Describe the morphology of the erythrocytes.
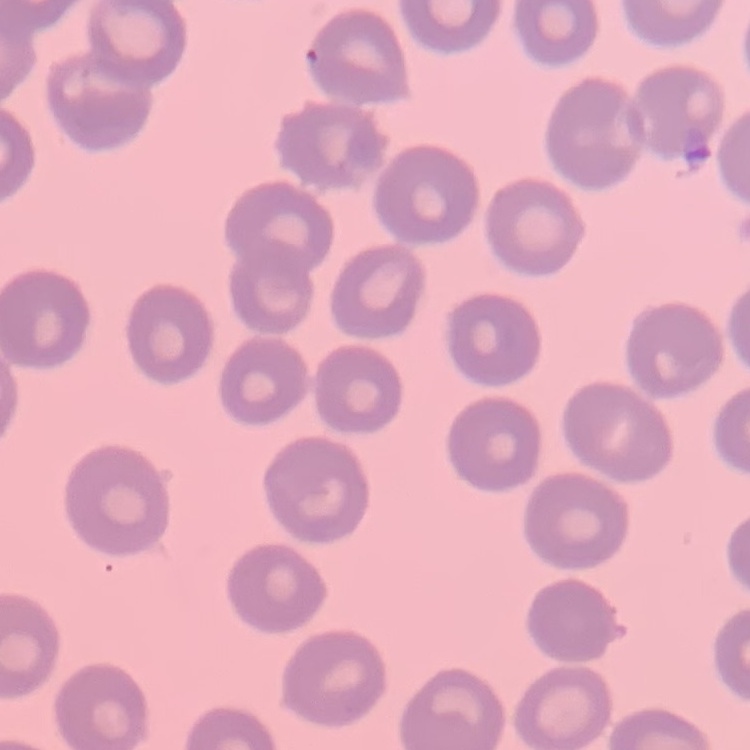
They show no rouleaux formation.

Thin peripheral smear. Field's or Giemsa stain. One tile cut from a larger photomicrograph.